Point out each malaria parasite.
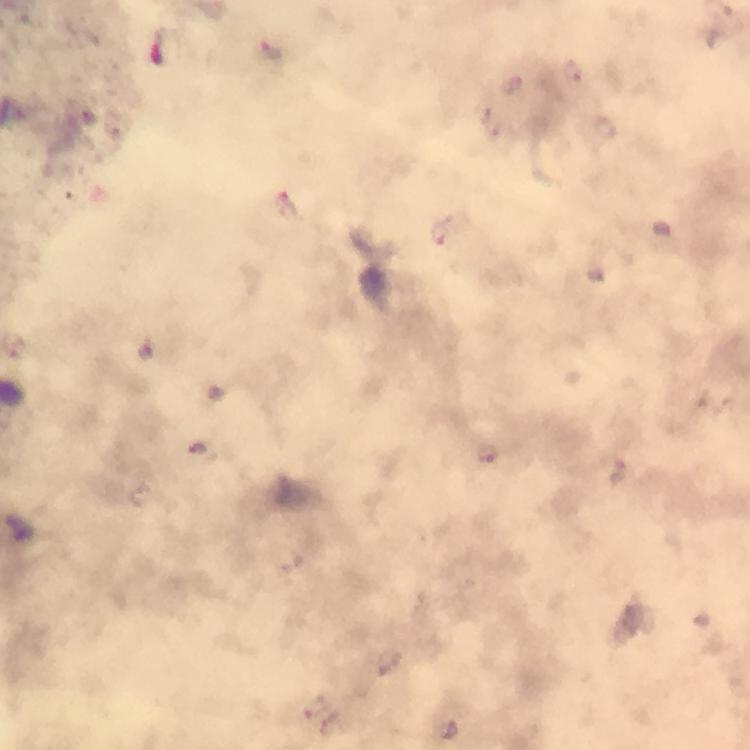
Approximate centers as (x, y) in pixels.
Malaria parasites: (271, 49), (573, 72), (198, 447), (487, 453), (315, 705).

Summary:
  - Immersion oil: applied
  - Magnification: 100x
  - Capture: smartphone camera through the microscope
  - Cropped from: one field of view
  - Stain: Giemsa
  - Image size: 750×750 pixels
  - Context: from a diagnostic examination for malaria
  - Preparation: thick blood smear